Assess the morphology of the red blood cells.
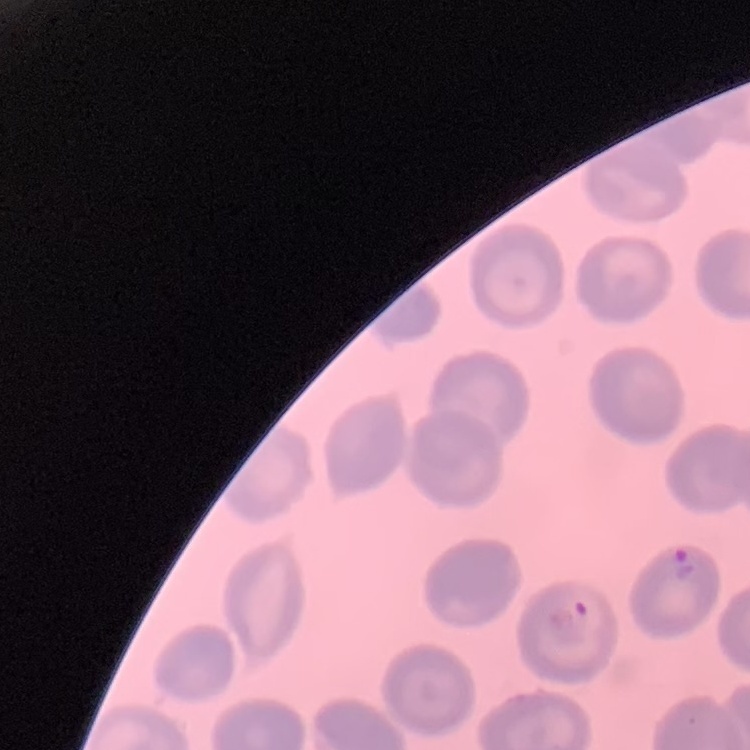
They show no rouleaux formation.

{
  "image_type": "square crop of a larger photomicrograph",
  "preparation": "thin blood film",
  "stain": "Field's or Giemsa"
}